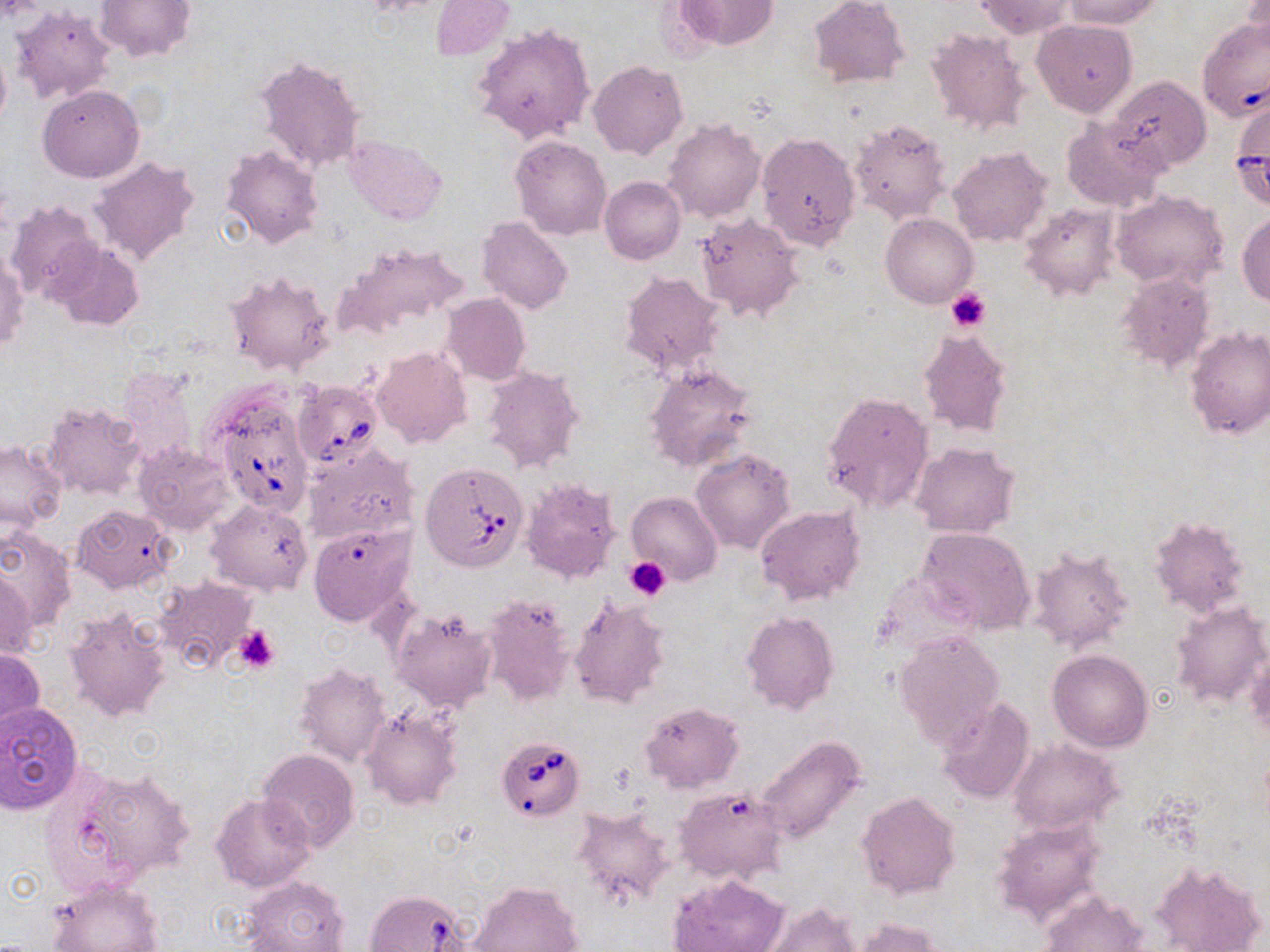
Approximate bounding boxes as [x1, y1, x2, y2] in pixels. Platelet locations: [946, 289, 992, 333], [623, 556, 671, 600], [234, 625, 282, 672]. Babesia divergens-infected red blood cell locations: [1196, 23, 1270, 121], [293, 381, 382, 468], [209, 387, 315, 518], [421, 463, 530, 572], [495, 736, 585, 821], [364, 889, 471, 952]. Uninfected red blood cell locations: [94, 0, 194, 61], [807, 0, 909, 88], [974, 0, 1077, 38], [1059, 0, 1165, 29], [1240, 0, 1269, 60], [674, 1, 778, 50], [431, 2, 513, 59], [10, 5, 115, 105], [1032, 19, 1137, 117], [472, 21, 597, 145], [926, 28, 1031, 138], [0, 39, 11, 132], [254, 53, 366, 174], [588, 60, 687, 159], [1109, 75, 1211, 172], [38, 84, 144, 182], [661, 117, 765, 223], [1061, 117, 1170, 212], [850, 118, 950, 223], [757, 132, 860, 251], [343, 135, 445, 225], [512, 136, 612, 239], [222, 145, 325, 248], [948, 147, 1051, 246], [90, 157, 199, 267], [599, 177, 684, 265], [1111, 189, 1227, 290], [6, 199, 100, 304], [1021, 203, 1118, 299], [696, 211, 802, 321], [1237, 211, 1270, 307], [881, 213, 977, 307], [478, 217, 574, 315], [332, 240, 469, 341], [49, 242, 145, 331], [1, 247, 27, 354], [224, 270, 335, 376], [619, 271, 728, 380], [1117, 271, 1217, 375], [441, 293, 531, 385], [1184, 326, 1270, 440], [918, 327, 1012, 436], [371, 347, 471, 449], [643, 363, 756, 472], [118, 365, 201, 465], [481, 365, 585, 473], [822, 391, 935, 513], [42, 401, 147, 501], [0, 441, 66, 531], [133, 442, 234, 535], [909, 443, 1019, 537], [303, 445, 419, 545], [691, 448, 794, 554], [520, 478, 622, 586], [627, 492, 722, 585], [206, 498, 313, 596], [72, 504, 176, 595], [755, 505, 866, 606], [1149, 515, 1250, 616], [308, 522, 416, 625], [917, 527, 1035, 633], [0, 528, 77, 634], [1026, 545, 1135, 654], [1, 566, 38, 661], [154, 577, 257, 673], [479, 593, 577, 707], [568, 596, 671, 708], [1169, 599, 1269, 708], [389, 607, 496, 712], [63, 609, 170, 722], [741, 612, 838, 716], [895, 630, 1005, 749], [0, 646, 43, 742], [1245, 646, 1269, 743], [1048, 650, 1153, 753], [294, 662, 392, 768], [937, 696, 1036, 805], [0, 702, 84, 813], [640, 702, 743, 793], [362, 707, 464, 810], [754, 736, 867, 847], [1008, 739, 1122, 834], [257, 749, 360, 851], [51, 764, 194, 887], [676, 786, 788, 885], [211, 792, 315, 892], [856, 792, 961, 899], [572, 805, 676, 908], [992, 816, 1109, 925], [1152, 862, 1264, 952], [668, 873, 787, 952], [240, 875, 351, 951], [46, 876, 164, 952], [470, 880, 583, 952], [1040, 889, 1147, 952], [758, 902, 860, 952], [850, 918, 945, 952]. Slide-level diagnosis: Babesia divergens. Image is 1270×952 pixels. Thin blood film. Single field of view. May-Grünwald-Giemsa stain. Captured at 1000x magnification. Optical microscopy.